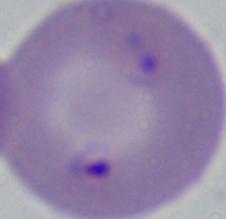

Summary:
  - Identification: Babesia
  - Magnification: 1000x
  - Modality: micrograph